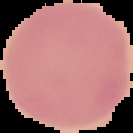

Summary:
  - Preparation: thin blood film
  - Image size: 133×133 pixels
  - Image type: cell region segmented out of the field of view; surrounding area masked to black
  - Malaria status: uninfected